Locate every Plasmodium falciparum-infected red blood cell.
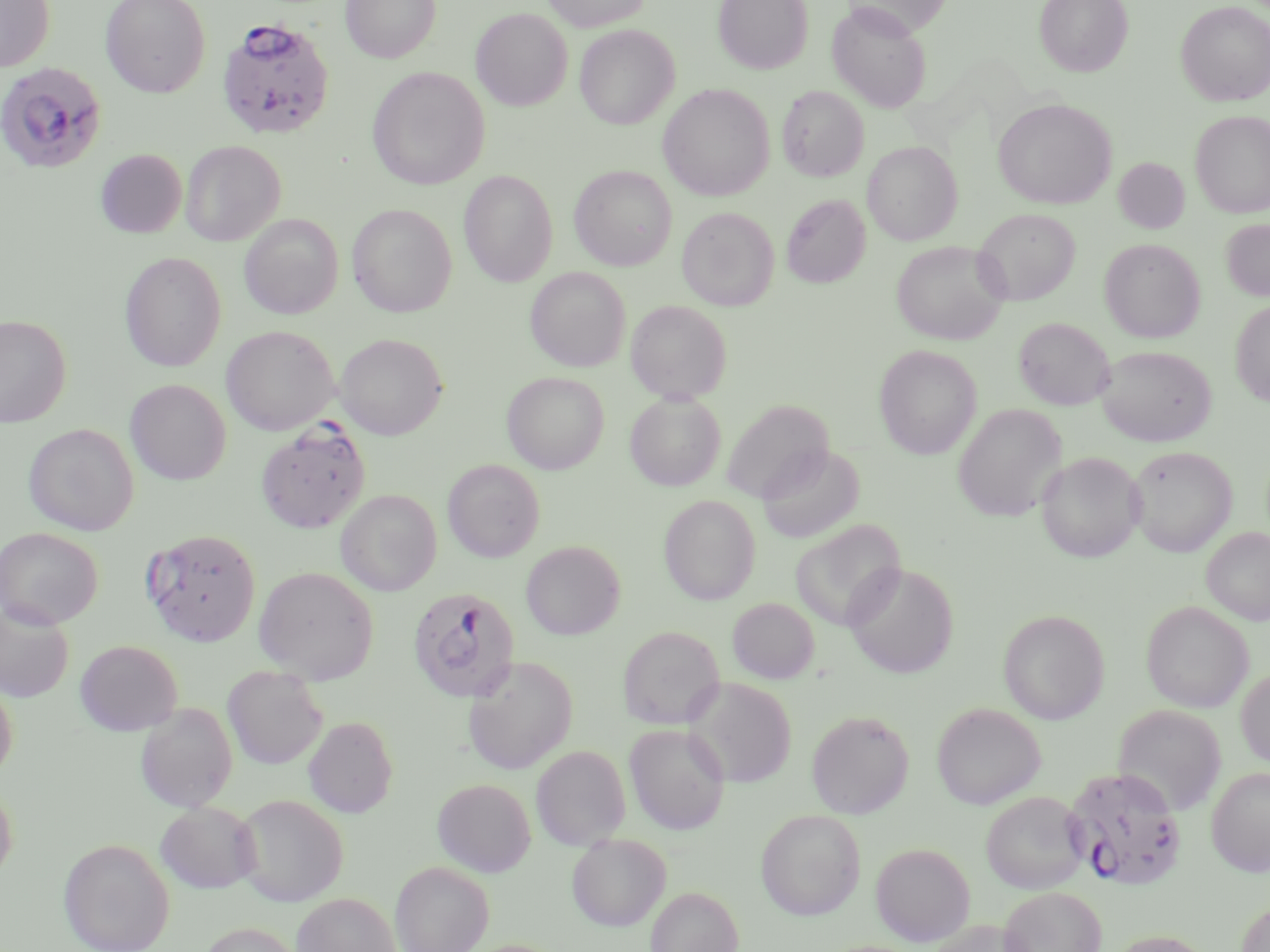
Approximate bounding boxes as [x1, y1, x2, y2] in pixels.
Plasmodium falciparum-infected red blood cells: [216, 16, 335, 140], [0, 62, 107, 175], [407, 587, 521, 704], [1062, 767, 1187, 891].

Summary:
  - Uninfected red blood cell locations: [0, 0, 54, 72], [100, 0, 210, 98], [341, 0, 441, 63], [541, 0, 651, 31], [713, 0, 813, 74], [841, 0, 952, 35], [1034, 0, 1133, 76], [1175, 1, 1270, 106], [827, 3, 931, 113], [471, 8, 573, 110], [574, 24, 679, 130], [367, 67, 490, 190], [658, 84, 775, 201], [777, 85, 868, 182], [993, 98, 1117, 210], [1190, 110, 1270, 218], [180, 140, 285, 246], [863, 140, 962, 245], [95, 149, 187, 238], [1113, 157, 1190, 234], [570, 165, 677, 271], [459, 169, 558, 287], [781, 194, 870, 288], [347, 204, 457, 317], [677, 207, 779, 310], [973, 208, 1080, 305], [239, 214, 344, 319], [1221, 218, 1270, 301], [1100, 239, 1205, 342], [890, 240, 1010, 345], [120, 252, 226, 371], [526, 267, 631, 371], [625, 300, 732, 403], [1230, 300, 1270, 407], [0, 314, 71, 427], [1014, 317, 1115, 410], [221, 326, 339, 435], [335, 333, 448, 440], [874, 344, 982, 459], [1096, 345, 1216, 446], [502, 372, 609, 474], [125, 379, 231, 485], [625, 391, 726, 491], [721, 399, 834, 502], [953, 404, 1067, 522], [257, 421, 371, 533], [23, 423, 139, 535], [756, 443, 864, 545], [1127, 445, 1237, 556], [1036, 452, 1144, 562], [443, 458, 545, 562], [336, 489, 441, 596], [658, 494, 761, 605], [791, 519, 906, 631], [0, 527, 103, 629], [1201, 527, 1270, 625], [141, 528, 261, 646], [521, 541, 625, 640], [843, 562, 959, 678], [254, 566, 379, 685], [727, 598, 819, 684], [1141, 600, 1253, 713], [0, 601, 74, 703], [998, 609, 1110, 724], [617, 625, 725, 729], [75, 640, 183, 736], [463, 656, 578, 774], [223, 666, 327, 769], [1236, 667, 1270, 769], [0, 676, 18, 783], [685, 677, 796, 787], [135, 702, 238, 812], [932, 702, 1045, 809], [1113, 705, 1227, 816], [806, 709, 914, 818], [304, 716, 399, 818], [624, 723, 731, 834], [531, 745, 631, 850], [1206, 767, 1270, 876], [432, 778, 536, 876], [0, 780, 18, 886], [981, 791, 1090, 895], [233, 793, 349, 906], [155, 801, 260, 893], [755, 808, 865, 920], [566, 832, 671, 931], [58, 837, 175, 952], [871, 842, 975, 946], [390, 861, 493, 952], [646, 885, 743, 952], [999, 886, 1106, 952], [291, 893, 401, 952], [1236, 901, 1270, 952], [929, 918, 1036, 952], [196, 922, 306, 952], [1106, 929, 1217, 952]
  - Slide-level diagnosis: Plasmodium falciparum
  - Modality: optical microscopy
  - Stain: May-Grünwald-Giemsa
  - Magnification: 1000x
  - Preparation: thin blood smear
  - Field of view: single
  - Image size: 1270×952 pixels